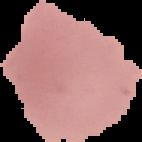 Malaria status: uninfected. From a thin blood smear. Image is 142×142 pixels. Cell region segmented out of the field of view; the surrounding area is masked to black.